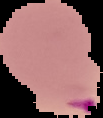
Segmented cell region on a black background. Image is 103×118 pixels. From a thin blood film. Malaria status: parasitized.